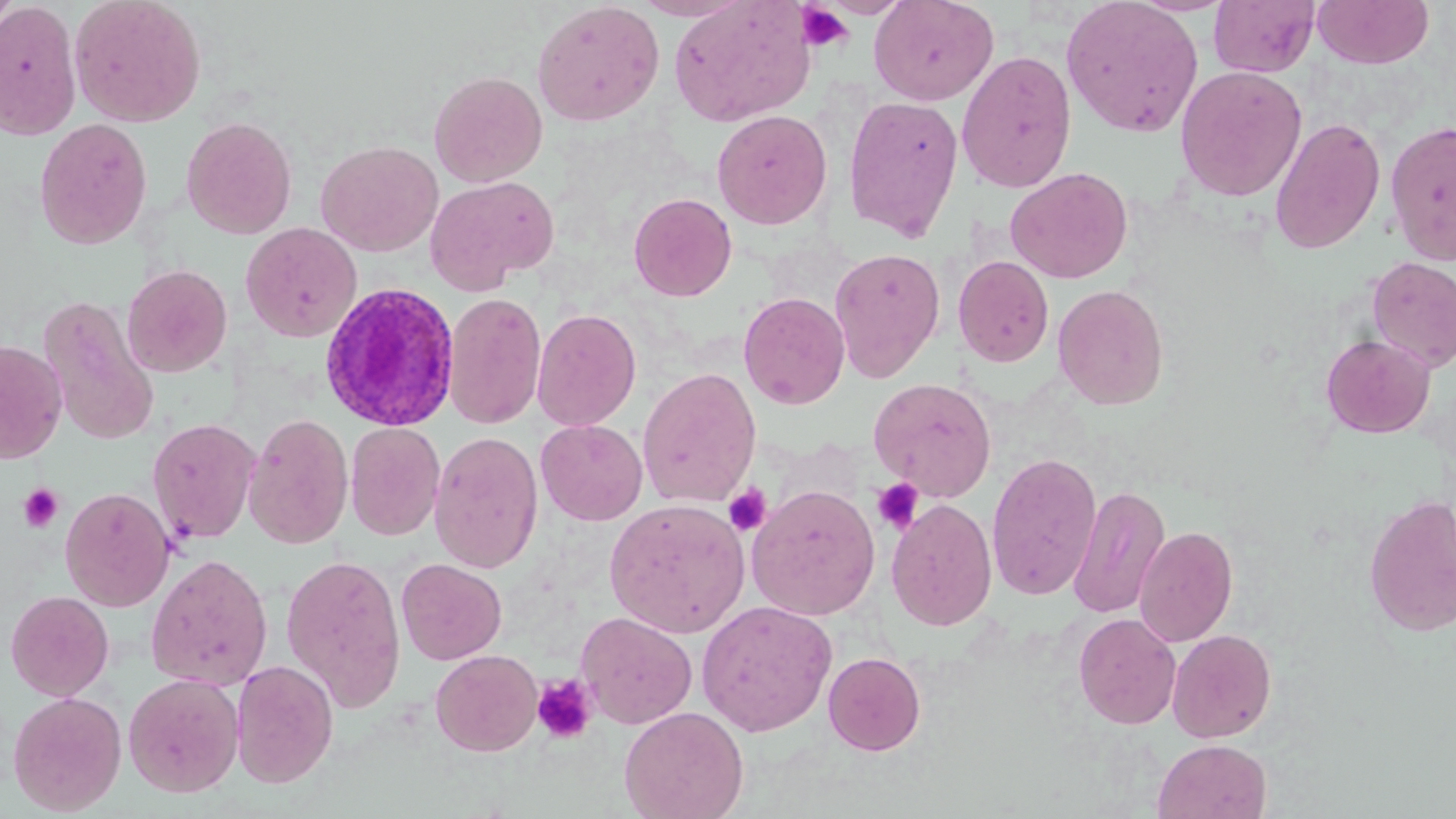

Approximate bounding boxes as named x1/y1/x2/y2 corners in pixels. Plasmodium ovale-infected red blood cell locations: (x1=318, y1=282, x2=460, y2=433). Platelet locations: (x1=795, y1=2, x2=855, y2=53), (x1=872, y1=478, x2=924, y2=534), (x1=19, y1=483, x2=63, y2=533), (x1=723, y1=483, x2=773, y2=536), (x1=532, y1=674, x2=597, y2=744). Uninfected red blood cell locations: (x1=0, y1=0, x2=20, y2=35), (x1=69, y1=0, x2=206, y2=127), (x1=668, y1=0, x2=817, y2=127), (x1=869, y1=0, x2=999, y2=106), (x1=1060, y1=0, x2=1204, y2=137), (x1=1209, y1=0, x2=1319, y2=78), (x1=1312, y1=0, x2=1434, y2=70), (x1=531, y1=1, x2=665, y2=127), (x1=0, y1=3, x2=81, y2=140), (x1=956, y1=49, x2=1077, y2=193), (x1=1174, y1=65, x2=1308, y2=201), (x1=428, y1=70, x2=547, y2=187), (x1=842, y1=95, x2=964, y2=242), (x1=711, y1=109, x2=833, y2=230), (x1=181, y1=116, x2=297, y2=239), (x1=1269, y1=117, x2=1386, y2=255), (x1=34, y1=118, x2=153, y2=250), (x1=1385, y1=120, x2=1456, y2=266), (x1=315, y1=140, x2=443, y2=256), (x1=1005, y1=166, x2=1134, y2=283), (x1=425, y1=175, x2=559, y2=292), (x1=628, y1=192, x2=737, y2=302), (x1=241, y1=222, x2=362, y2=343), (x1=828, y1=248, x2=946, y2=382), (x1=953, y1=255, x2=1054, y2=367), (x1=1367, y1=257, x2=1456, y2=371), (x1=122, y1=264, x2=232, y2=378), (x1=1052, y1=284, x2=1170, y2=410), (x1=443, y1=291, x2=546, y2=430), (x1=738, y1=292, x2=850, y2=410), (x1=39, y1=296, x2=161, y2=445), (x1=531, y1=308, x2=642, y2=431), (x1=1320, y1=334, x2=1435, y2=438), (x1=0, y1=339, x2=67, y2=464), (x1=637, y1=368, x2=761, y2=508), (x1=868, y1=377, x2=998, y2=501), (x1=243, y1=412, x2=353, y2=549), (x1=147, y1=417, x2=262, y2=545), (x1=535, y1=420, x2=648, y2=525), (x1=345, y1=422, x2=445, y2=541), (x1=429, y1=431, x2=544, y2=574), (x1=986, y1=451, x2=1103, y2=602), (x1=746, y1=484, x2=881, y2=620), (x1=1068, y1=484, x2=1170, y2=619), (x1=60, y1=486, x2=175, y2=612), (x1=1363, y1=494, x2=1456, y2=637), (x1=604, y1=498, x2=751, y2=638), (x1=886, y1=499, x2=997, y2=632), (x1=1134, y1=525, x2=1239, y2=647), (x1=281, y1=552, x2=407, y2=712), (x1=146, y1=554, x2=273, y2=690), (x1=396, y1=558, x2=507, y2=665), (x1=4, y1=590, x2=114, y2=700), (x1=696, y1=600, x2=837, y2=737), (x1=576, y1=611, x2=697, y2=729), (x1=1073, y1=613, x2=1181, y2=729), (x1=1167, y1=628, x2=1277, y2=743), (x1=430, y1=649, x2=543, y2=756), (x1=823, y1=652, x2=926, y2=755), (x1=231, y1=659, x2=339, y2=788), (x1=123, y1=673, x2=245, y2=797), (x1=7, y1=691, x2=127, y2=815), (x1=619, y1=706, x2=749, y2=819), (x1=1153, y1=738, x2=1272, y2=819). Slide-level diagnosis: Plasmodium ovale. Thin blood smear. 1000x magnification. Image is 1456×819 pixels. Single field of view. May-Grünwald-Giemsa-stained preparation. Light microscopy.